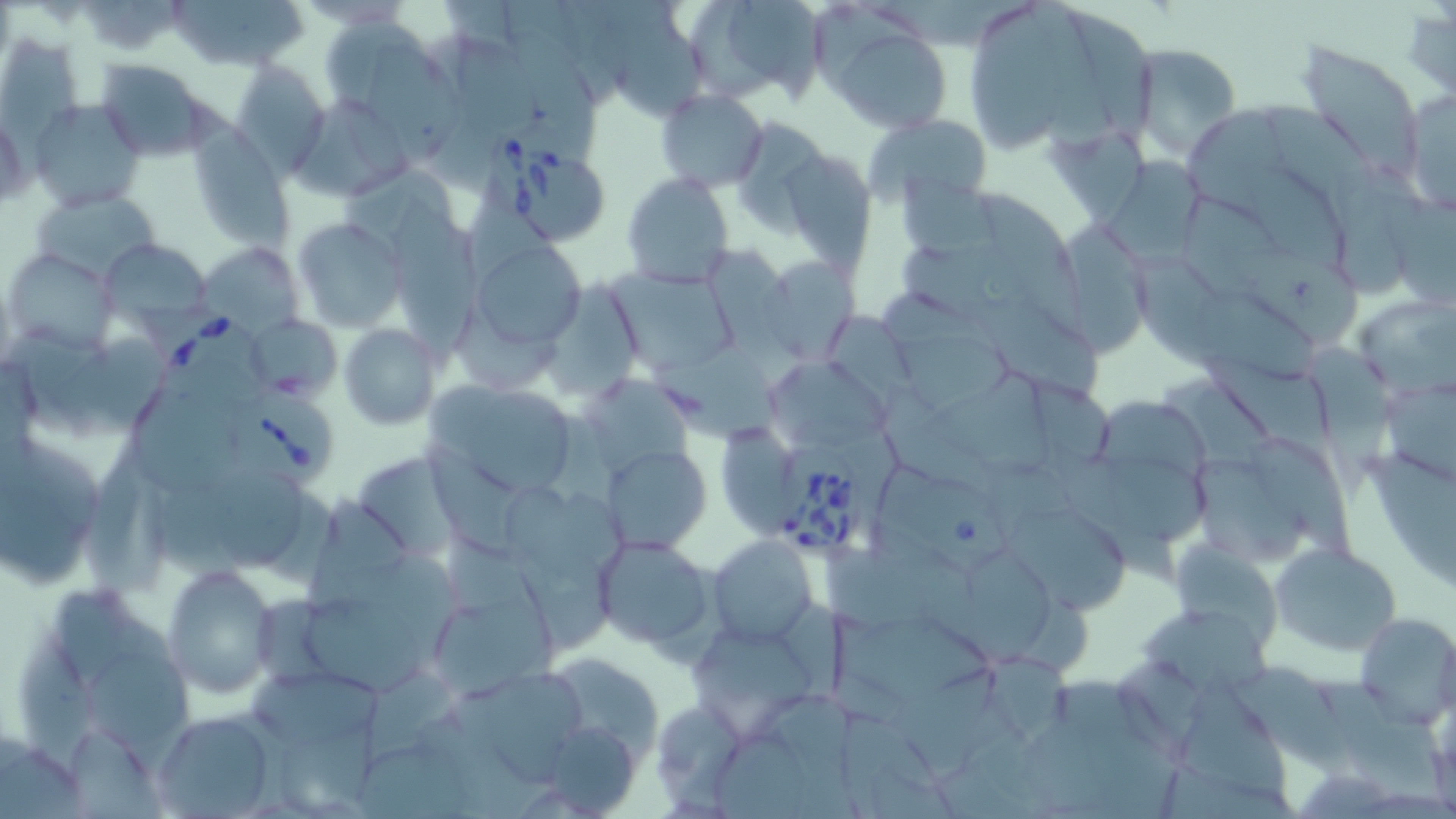

slide_level_diagnosis: Babesia divergens
field_of_view: one of a larger specimen
preparation: thin blood smear
modality: optical microscopy
uninfected_red_blood_cell_locations: 'approximate bounding boxes as (x1, y1, x2, y2) in pixels: (168, 0, 307, 73), (686, 0, 829, 105), (1024, 1, 1117, 151), (977, 8, 1063, 157), (1069, 10, 1156, 147), (607, 15, 706, 119), (323, 16, 429, 100), (446, 25, 544, 128), (826, 25, 954, 132), (510, 32, 600, 158), (0, 33, 83, 142), (1126, 41, 1242, 160), (1298, 42, 1426, 179), (374, 45, 462, 162), (94, 59, 219, 159), (231, 62, 331, 176), (1399, 87, 1455, 219), (657, 89, 768, 191), (295, 94, 413, 203), (30, 99, 147, 215), (1189, 108, 1286, 217), (863, 112, 993, 207), (0, 113, 30, 214), (728, 117, 828, 228), (188, 127, 294, 249), (780, 151, 875, 271), (1098, 157, 1211, 277), (338, 162, 460, 253), (1249, 167, 1345, 273), (622, 172, 734, 288), (898, 173, 997, 259), (1334, 177, 1413, 303), (974, 186, 1091, 338), (32, 190, 159, 283), (392, 194, 480, 363), (1183, 194, 1281, 298), (292, 216, 406, 336), (1060, 217, 1161, 356), (98, 236, 213, 331), (469, 240, 587, 353), (196, 242, 301, 335), (707, 244, 800, 359), (1222, 247, 1360, 347), (9, 249, 117, 352), (1128, 250, 1240, 369), (762, 256, 859, 364), (616, 273, 744, 376), (554, 282, 641, 403), (978, 286, 1103, 402), (1196, 291, 1323, 387), (1354, 292, 1456, 395), (453, 312, 565, 388), (248, 314, 342, 402), (340, 324, 441, 431), (44, 335, 164, 442), (899, 335, 1014, 413), (656, 342, 779, 437), (1202, 347, 1340, 466), (1306, 347, 1399, 500), (765, 364, 893, 450), (583, 368, 694, 471), (931, 372, 1060, 482), (426, 380, 583, 499), (1382, 380, 1456, 480), (133, 389, 236, 501), (1094, 400, 1209, 486), (0, 428, 108, 591), (1246, 434, 1356, 559), (418, 436, 523, 555), (603, 443, 711, 551), (1052, 447, 1211, 545), (354, 450, 462, 562), (1362, 453, 1456, 592), (1192, 458, 1312, 567), (874, 466, 1015, 574), (215, 471, 305, 566), (503, 482, 629, 586), (158, 486, 242, 584), (307, 492, 412, 610), (999, 498, 1130, 611), (709, 536, 817, 647), (590, 537, 715, 653), (1175, 540, 1279, 653), (1270, 541, 1402, 657), (968, 546, 1055, 668), (823, 547, 973, 640), (520, 551, 614, 655), (380, 555, 462, 667), (163, 563, 281, 698), (53, 588, 169, 682), (254, 593, 332, 685), (442, 597, 552, 701), (304, 599, 424, 698), (1143, 608, 1269, 700), (829, 611, 994, 702), (1355, 612, 1456, 728), (692, 631, 819, 707), (19, 632, 96, 762), (981, 648, 1075, 743), (88, 654, 193, 746), (548, 654, 666, 761), (1234, 665, 1357, 778), (897, 667, 1002, 780), (480, 669, 583, 786), (366, 670, 459, 764), (245, 671, 385, 743), (1320, 682, 1447, 802), (655, 694, 744, 812), (150, 710, 279, 818), (839, 713, 959, 819), (277, 717, 380, 817), (1016, 718, 1183, 816), (552, 724, 641, 816), (716, 728, 806, 819), (68, 729, 165, 819), (0, 741, 91, 819), (358, 746, 472, 819), (1157, 759, 1293, 819)'
image_size: 1456×819 pixels
magnification: 1000x
stain: May-Grünwald-Giemsa
babesia_divergens_infected_red_blood_cell_locations: 'approximate bounding boxes as (x1, y1, x2, y2) in pixels: (490, 139, 611, 246), (135, 297, 280, 403), (224, 386, 337, 488), (766, 450, 861, 562)'